Name the parasite shown.
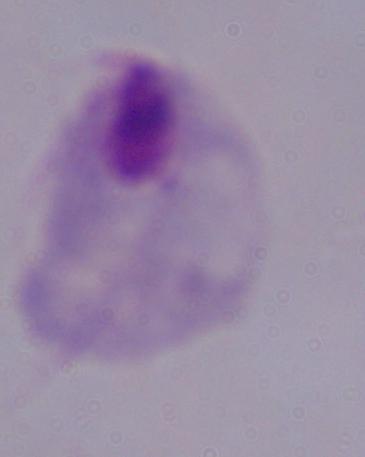
This is a trichomonad.

modality = photomicrograph
magnification = 1000x